Report the malaria status of this cell.
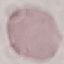

Uninfected.

Summary:
  - Image type: cell patch, automatically extracted from a larger field of view and resized to 64 × 64 pixels
  - Preparation: thin blood film
  - Capture: smartphone through the microscope eyepiece
  - Stain: Giemsa